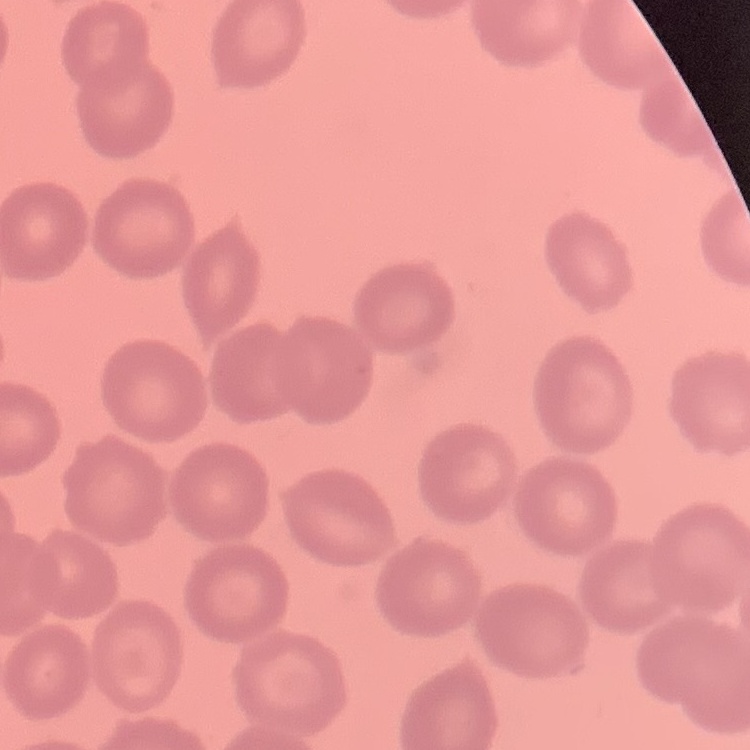
erythrocyte morphology = no rouleaux formation
image type = one tile cut from a larger photomicrograph
preparation = thin peripheral smear
stain = Field's or Giemsa